Classify this cell by malaria status.
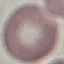
It is uninfected.

Giemsa-stained preparation. Acquired by smartphone through the microscope eyepiece. Thin smear of blood. Cell patch, automatically extracted from a larger field of view and resized to 64 × 64 pixels.